Report the malaria status of this cell.
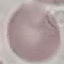
It is uninfected.

stain = Giemsa
preparation = thin blood smear
capture = smartphone through the microscope eyepiece
image type = cell patch, automatically extracted from a larger field of view and resized to 64 × 64 pixels